Locate every blood parasite and identify its species.
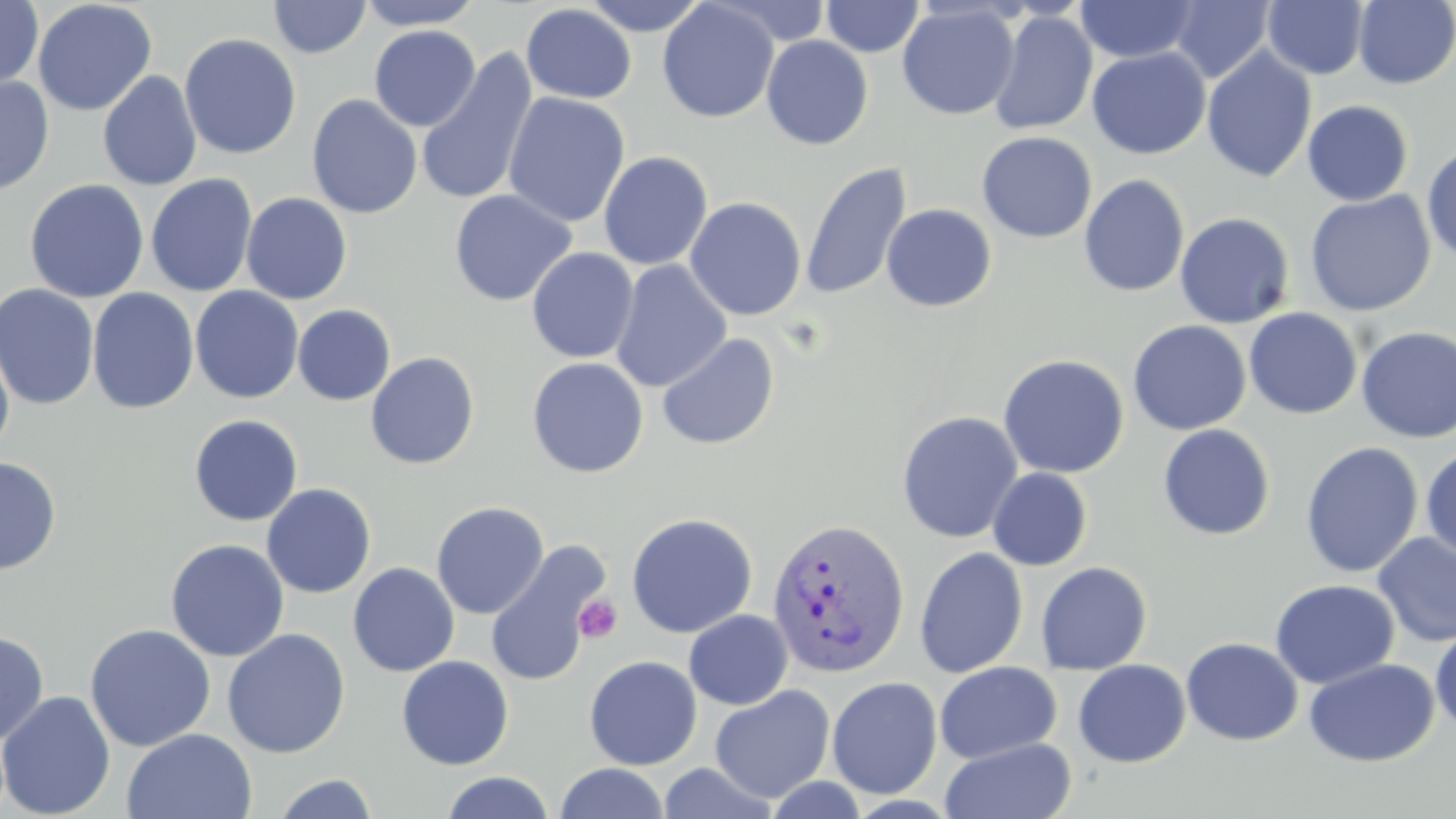

Approximate bounding boxes as (x1,y1)-(x2,y2) corner pairs in pixels.
Plasmodium vivax-infected red blood cells: (766,517)-(910,680).
No Plasmodium falciparum, Plasmodium ovale, Plasmodium malariae, Babesia divergens, or Trypanosoma brucei observed.

{
  "slide_level_diagnosis": "Plasmodium vivax",
  "magnification": "1000x",
  "modality": "light microscopy",
  "image_size": "1456×819 pixels",
  "platelet_locations": "approximate bounding boxes as (x1,y1)-(x2,y2) corner pairs in pixels: (573,594)-(622,643)",
  "uninfected_red_blood_cell_locations": "approximate bounding boxes as (x1,y1)-(x2,y2) corner pairs in pixels: (0,0)-(43,91), (268,0)-(371,59), (354,0)-(485,30), (581,0)-(710,35), (821,0)-(925,58), (1263,0)-(1369,79), (1353,0)-(1455,89), (32,1)-(157,116), (657,1)-(779,123), (1076,1)-(1199,63), (1170,1)-(1273,83), (520,3)-(637,104), (896,3)-(1020,120), (988,10)-(1098,135), (368,25)-(481,132), (179,33)-(302,160), (761,34)-(873,151), (1087,47)-(1210,159), (1201,47)-(1317,182), (416,49)-(539,206), (97,70)-(202,191), (0,75)-(54,196), (503,92)-(630,227), (306,94)-(423,219), (1302,100)-(1414,206), (976,131)-(1098,243), (1421,143)-(1456,263), (598,151)-(713,270), (800,161)-(912,300), (145,173)-(258,297), (1079,174)-(1190,297), (24,179)-(149,303), (449,189)-(576,307), (1305,190)-(1436,316), (241,192)-(352,304), (684,196)-(807,321), (881,203)-(997,312), (1174,212)-(1295,328), (526,248)-(638,363), (610,260)-(732,392), (0,283)-(100,410), (190,285)-(304,404), (87,287)-(199,415), (292,304)-(396,406), (1244,308)-(1362,419), (1127,320)-(1251,435), (1356,327)-(1456,443), (656,332)-(780,451), (0,335)-(15,459), (365,351)-(480,470), (998,354)-(1129,479), (527,357)-(649,478), (896,410)-(1023,544), (189,414)-(303,526), (1157,424)-(1275,541), (1300,441)-(1423,578), (1420,446)-(1456,563), (0,456)-(61,575), (987,467)-(1092,571), (261,483)-(376,598), (431,501)-(549,619), (626,512)-(758,638), (1373,533)-(1456,648), (165,539)-(290,662), (485,541)-(609,688), (914,546)-(1029,678), (1035,561)-(1153,675), (348,562)-(460,677), (1270,579)-(1400,689), (684,609)-(793,710), (84,623)-(216,752), (1430,626)-(1456,735), (222,627)-(351,758), (0,630)-(49,746), (1181,637)-(1303,746), (396,655)-(514,770), (584,655)-(702,771), (1304,658)-(1439,767), (1073,659)-(1191,767), (934,661)-(1062,764), (826,677)-(942,799), (709,684)-(835,803), (0,690)-(116,818), (122,728)-(257,818), (940,737)-(1077,819), (656,762)-(780,819), (554,763)-(670,819), (440,771)-(555,819), (273,773)-(380,819)",
  "stain": "May-Grünwald-Giemsa",
  "field_of_view": "single",
  "preparation": "thin blood smear"
}